Locate every blood parasite and identify its species.
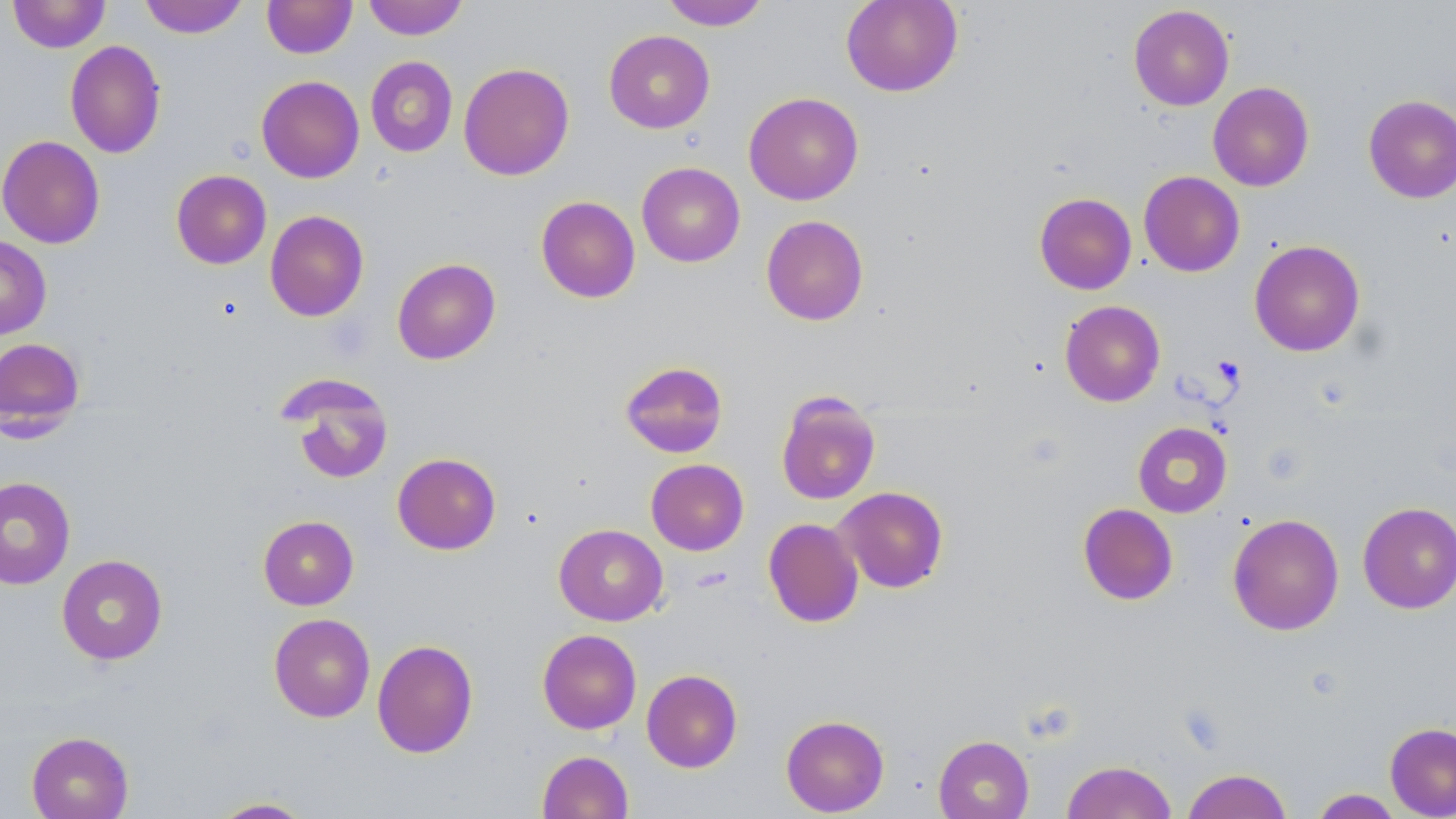

No blood parasites seen.

Approximate bounding boxes as named x1/y1/x2/y2 corners in pixels. Uninfected red blood cell locations: (x1=8, y1=0, x2=110, y2=52), (x1=139, y1=0, x2=249, y2=38), (x1=262, y1=0, x2=357, y2=58), (x1=363, y1=0, x2=468, y2=40), (x1=660, y1=0, x2=771, y2=30), (x1=841, y1=0, x2=963, y2=96), (x1=1128, y1=5, x2=1234, y2=110), (x1=604, y1=30, x2=715, y2=133), (x1=65, y1=40, x2=166, y2=158), (x1=365, y1=56, x2=458, y2=157), (x1=458, y1=62, x2=575, y2=180), (x1=256, y1=76, x2=364, y2=183), (x1=1208, y1=81, x2=1314, y2=191), (x1=743, y1=92, x2=864, y2=205), (x1=1363, y1=94, x2=1456, y2=203), (x1=0, y1=134, x2=106, y2=249), (x1=636, y1=162, x2=745, y2=267), (x1=171, y1=170, x2=272, y2=269), (x1=1139, y1=171, x2=1245, y2=277), (x1=1034, y1=192, x2=1136, y2=294), (x1=535, y1=196, x2=640, y2=303), (x1=265, y1=210, x2=369, y2=321), (x1=761, y1=215, x2=869, y2=325), (x1=0, y1=235, x2=52, y2=340), (x1=1249, y1=239, x2=1365, y2=357), (x1=392, y1=258, x2=501, y2=364), (x1=1060, y1=300, x2=1165, y2=406), (x1=0, y1=337, x2=86, y2=438), (x1=619, y1=360, x2=729, y2=458), (x1=279, y1=375, x2=395, y2=486), (x1=775, y1=391, x2=881, y2=505), (x1=1133, y1=422, x2=1232, y2=518), (x1=392, y1=452, x2=502, y2=555), (x1=645, y1=459, x2=749, y2=555), (x1=0, y1=476, x2=75, y2=589), (x1=834, y1=486, x2=949, y2=593), (x1=1357, y1=502, x2=1456, y2=613), (x1=1077, y1=503, x2=1178, y2=606), (x1=1227, y1=513, x2=1344, y2=635), (x1=258, y1=515, x2=359, y2=610), (x1=763, y1=518, x2=863, y2=628), (x1=554, y1=524, x2=668, y2=626), (x1=56, y1=554, x2=168, y2=665), (x1=269, y1=613, x2=375, y2=722), (x1=537, y1=629, x2=641, y2=734), (x1=371, y1=639, x2=478, y2=758), (x1=641, y1=669, x2=742, y2=772), (x1=780, y1=714, x2=889, y2=816), (x1=1385, y1=722, x2=1456, y2=818), (x1=26, y1=731, x2=134, y2=819), (x1=933, y1=734, x2=1034, y2=819), (x1=537, y1=750, x2=634, y2=819), (x1=1062, y1=760, x2=1177, y2=819), (x1=1182, y1=769, x2=1292, y2=819), (x1=1310, y1=788, x2=1404, y2=818), (x1=208, y1=797, x2=315, y2=818). Slide-level diagnosis: negative for blood parasites. Image is 1456×819 pixels. Captured at 1000x magnification. May-Grünwald-Giemsa-stained preparation. Thin blood smear. Single field of view. Light microscopy.